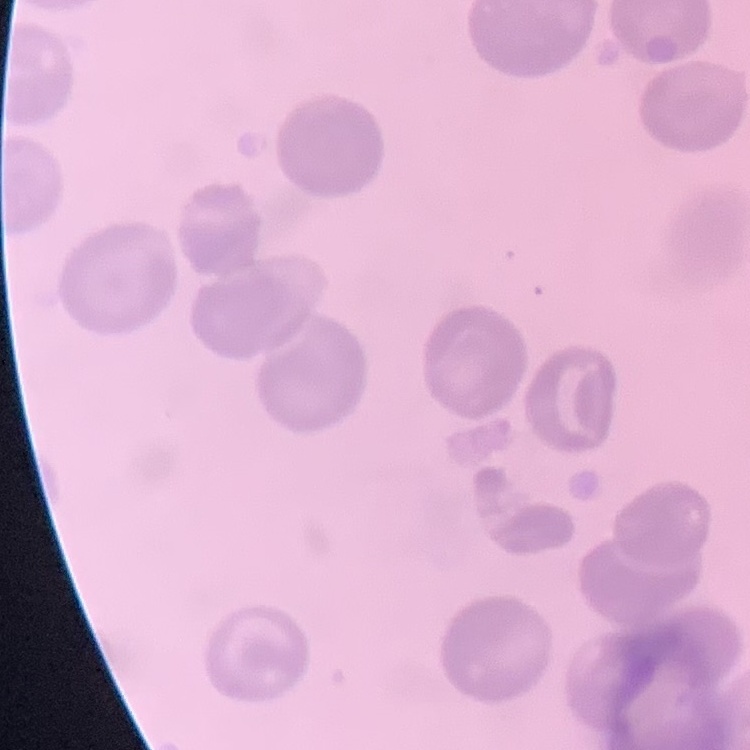

The erythrocytes exhibit no rouleaux formation. Thin blood smear. Field's or Giemsa stain. Square crop of a larger photomicrograph.